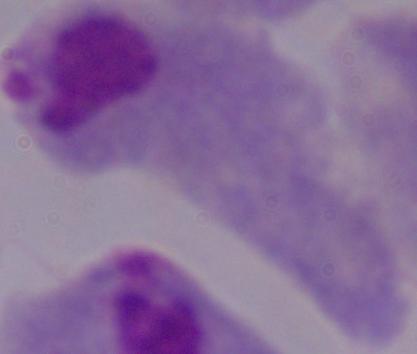

magnification = 1000x
modality = micrograph
identification = trichomonad